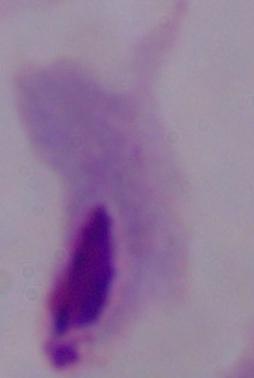

Summary:
  - Identification: trichomonad
  - Modality: photomicrograph
  - Magnification: 1000x